Comment on the morphology of the erythrocytes.
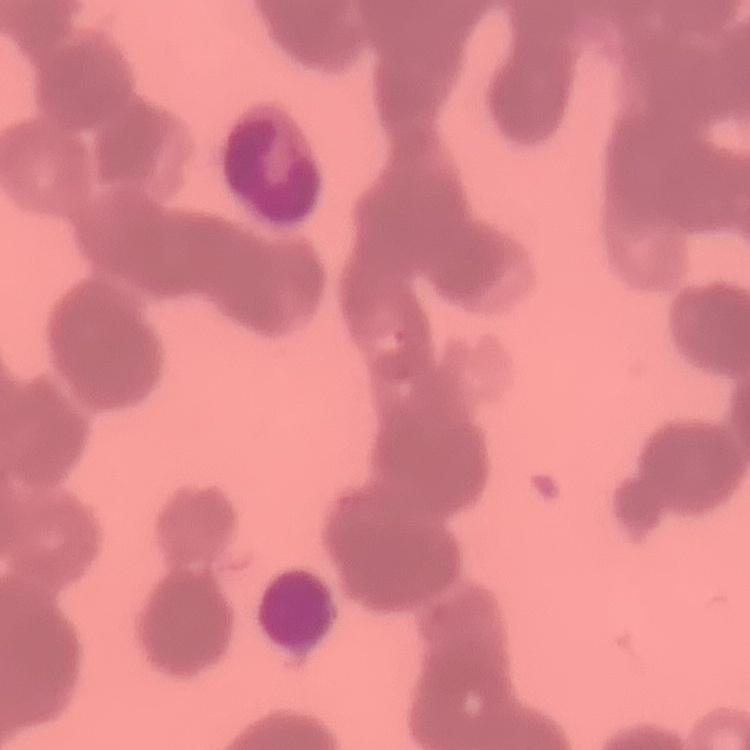
They show rouleaux formation.

One tile cut from a larger photomicrograph. Field's or Giemsa stain. Thin blood film.